Identify the parasite.
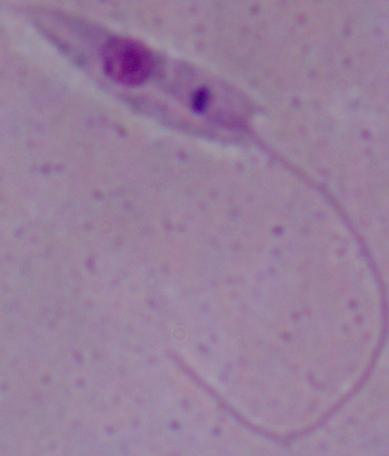
Leishmania.

Summary:
  - Modality: micrograph
  - Magnification: 1000x